Identify the parasite.
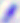

This is Toxoplasma gondii.

magnification = 400x
modality = micrograph